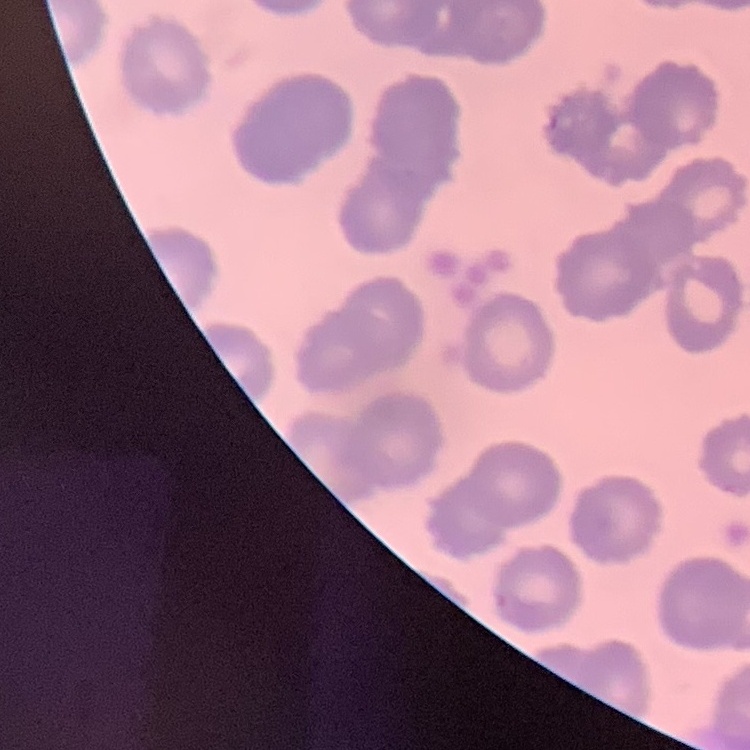

Summary:
  - Erythrocyte morphology: no rouleaux formation
  - Stain: Field's or Giemsa
  - Image type: one tile cut from a larger photomicrograph
  - Preparation: thin blood smear